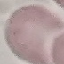
{
  "malaria_status": "uninfected",
  "image_type": "cell patch, automatically extracted from a larger field of view and resized to 64 × 64 pixels",
  "capture": "smartphone through the microscope eyepiece",
  "stain": "Giemsa",
  "preparation": "thin smear"
}